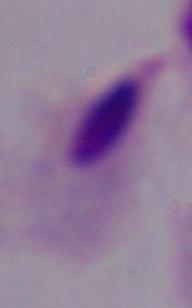

modality: micrograph
identification: trichomonad
magnification: 1000x